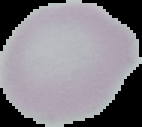

Summary:
  - Preparation: thin blood smear
  - Result: no Plasmodium parasites seen
  - Image type: segmented cell region with the area outside set to black
  - Image size: 142×127 pixels